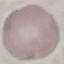

Summary:
  - Malaria status: uninfected
  - Image type: automatically extracted cell patch, resized to 64 × 64 pixels
  - Stain: Giemsa
  - Preparation: thin smear
  - Capture: smartphone camera at the microscope eyepiece